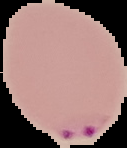
Summary:
  - Image type: segmented cell region on a black background
  - Preparation: thin blood smear
  - Result: malaria parasites identified
  - Image size: 127×148 pixels